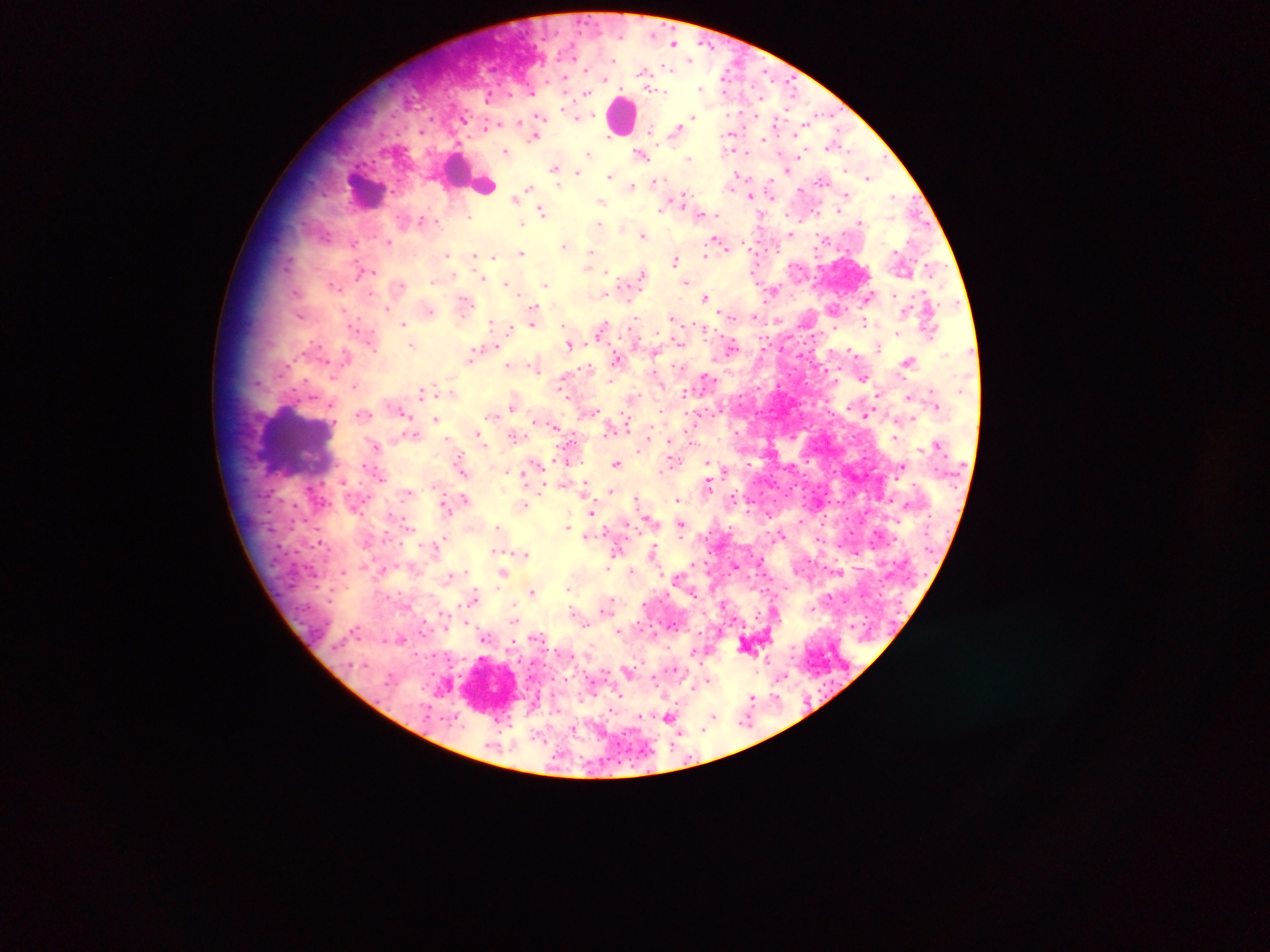
Approximate centers as [x, y] in pixels. Malaria parasite locations: [674, 43], [689, 59], [645, 72], [727, 73], [566, 79], [703, 88], [586, 93], [574, 113], [539, 116], [693, 116], [488, 126], [677, 130], [536, 135], [732, 137], [766, 139], [833, 144], [731, 145], [506, 152], [589, 153], [642, 155], [800, 155], [689, 158], [555, 168], [576, 170], [788, 170], [610, 176], [868, 176], [737, 177], [822, 180], [656, 181], [633, 187], [530, 188], [771, 188], [800, 189], [524, 191], [846, 194], [752, 195], [894, 196], [517, 198], [680, 199], [601, 202], [663, 208], [542, 211], [699, 212], [705, 213], [715, 214], [424, 219], [523, 221], [861, 221], [600, 225], [790, 234], [643, 235], [389, 241], [717, 241], [353, 243], [565, 245], [522, 252], [448, 254], [591, 255], [473, 256], [494, 256], [704, 257], [675, 258], [590, 263], [931, 267], [359, 270], [606, 273], [642, 274], [481, 278], [434, 279], [686, 281], [506, 283], [333, 284], [545, 284], [400, 285], [772, 290], [604, 294], [892, 295], [705, 297], [868, 297], [465, 301], [387, 308], [535, 308], [834, 308], [428, 309], [728, 314], [300, 315], [754, 316], [673, 318], [493, 322], [533, 322], [404, 323], [865, 323], [564, 325], [509, 328], [603, 328], [898, 332], [679, 342], [570, 343], [412, 344], [492, 346], [732, 347], [878, 348], [851, 350], [655, 352], [471, 357], [617, 360], [909, 360], [509, 365], [535, 366], [706, 377], [862, 377], [354, 384], [561, 388], [422, 391], [451, 392], [685, 393], [876, 396], [910, 396], [632, 397], [332, 403], [514, 403], [591, 412], [363, 413], [402, 413], [868, 414], [493, 415], [436, 418], [912, 418], [538, 421], [626, 425], [555, 426], [610, 429], [412, 434], [479, 435], [514, 435], [895, 438], [449, 439], [482, 440], [647, 440], [670, 441], [376, 446], [568, 460], [673, 461], [617, 464], [708, 464], [365, 465], [903, 466], [507, 470], [462, 471], [523, 472], [382, 477], [343, 481], [542, 485], [584, 485], [708, 485], [610, 490], [409, 492], [734, 496], [637, 497], [464, 499], [678, 499], [524, 504], [444, 506], [592, 511], [801, 519], [625, 522], [681, 523], [498, 526], [568, 527], [606, 530], [780, 534], [585, 535], [819, 539], [322, 542], [436, 544], [617, 550], [653, 551], [498, 552], [522, 552], [735, 565], [608, 566], [383, 568], [344, 570], [631, 570], [504, 572], [450, 575], [679, 576], [568, 589], [532, 591], [476, 597], [608, 603], [725, 604], [443, 614], [759, 614], [465, 621], [584, 622], [423, 628], [618, 630], [654, 633], [536, 636], [401, 638], [484, 638], [512, 640], [630, 669], [782, 675], [656, 678], [708, 681], [621, 696], [776, 696], [752, 697], [670, 717], [639, 718], [713, 718], [747, 720], [706, 725]. Leukocyte locations: [622, 116], [468, 174], [366, 188], [295, 441], [490, 688]. Photographed through a microscope with a mobile-phone camera. Collected in Ghana. Thick blood film. One field of view. Image is 1270×952 pixels.